Classify this cell by malaria status.
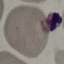

It is uninfected.

Thin blood film. Giemsa stain. Acquired by smartphone through the microscope eyepiece. Automatically extracted cell patch, resized to 64 × 64 pixels.